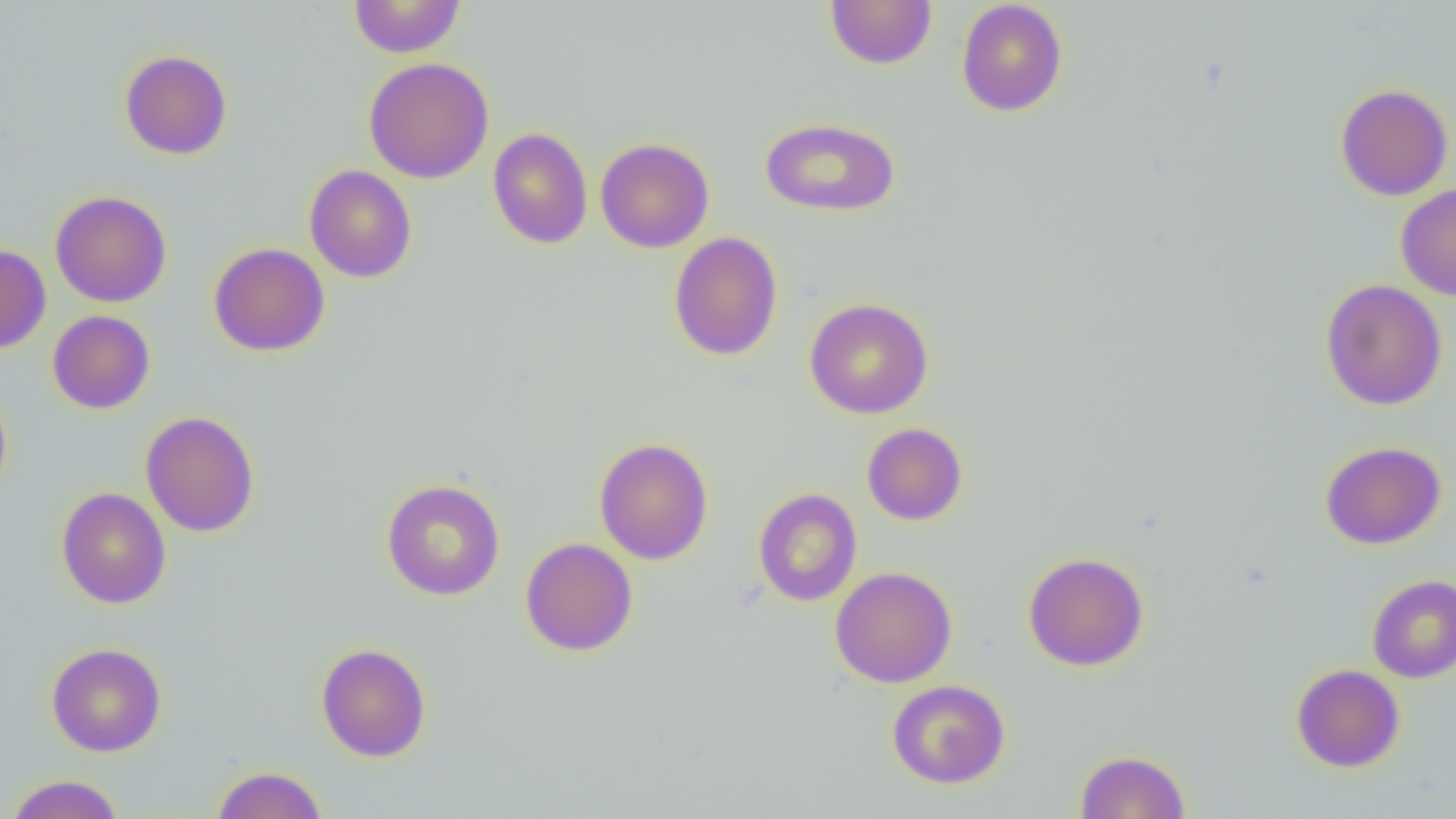

Approximate bounding boxes as [x1, y1, x2, y2] in pixels. Uninfected red blood cell locations: [348, 0, 465, 57], [825, 0, 937, 69], [956, 0, 1068, 117], [119, 49, 233, 160], [363, 57, 494, 183], [1335, 83, 1454, 200], [761, 117, 900, 216], [488, 127, 593, 249], [595, 138, 714, 253], [304, 165, 417, 283], [1395, 183, 1456, 300], [50, 190, 172, 307], [669, 231, 783, 361], [208, 242, 330, 357], [0, 244, 51, 354], [1320, 279, 1448, 410], [804, 297, 934, 419], [47, 310, 155, 414], [0, 381, 12, 502], [140, 411, 260, 537], [861, 422, 968, 526], [595, 437, 713, 564], [1320, 441, 1446, 549], [381, 478, 505, 600], [56, 487, 171, 608], [752, 488, 863, 606], [520, 538, 638, 656], [1023, 551, 1150, 671], [830, 566, 957, 688], [1366, 574, 1456, 683], [46, 642, 166, 756], [315, 642, 432, 762], [1291, 663, 1405, 773], [887, 679, 1011, 788], [1074, 749, 1191, 818], [211, 765, 327, 819], [5, 774, 124, 819]. Slide-level diagnosis: negative for blood parasites. Single field of view. Thin blood film. Light microscopy. 1000x magnification. Image is 1456×819 pixels.